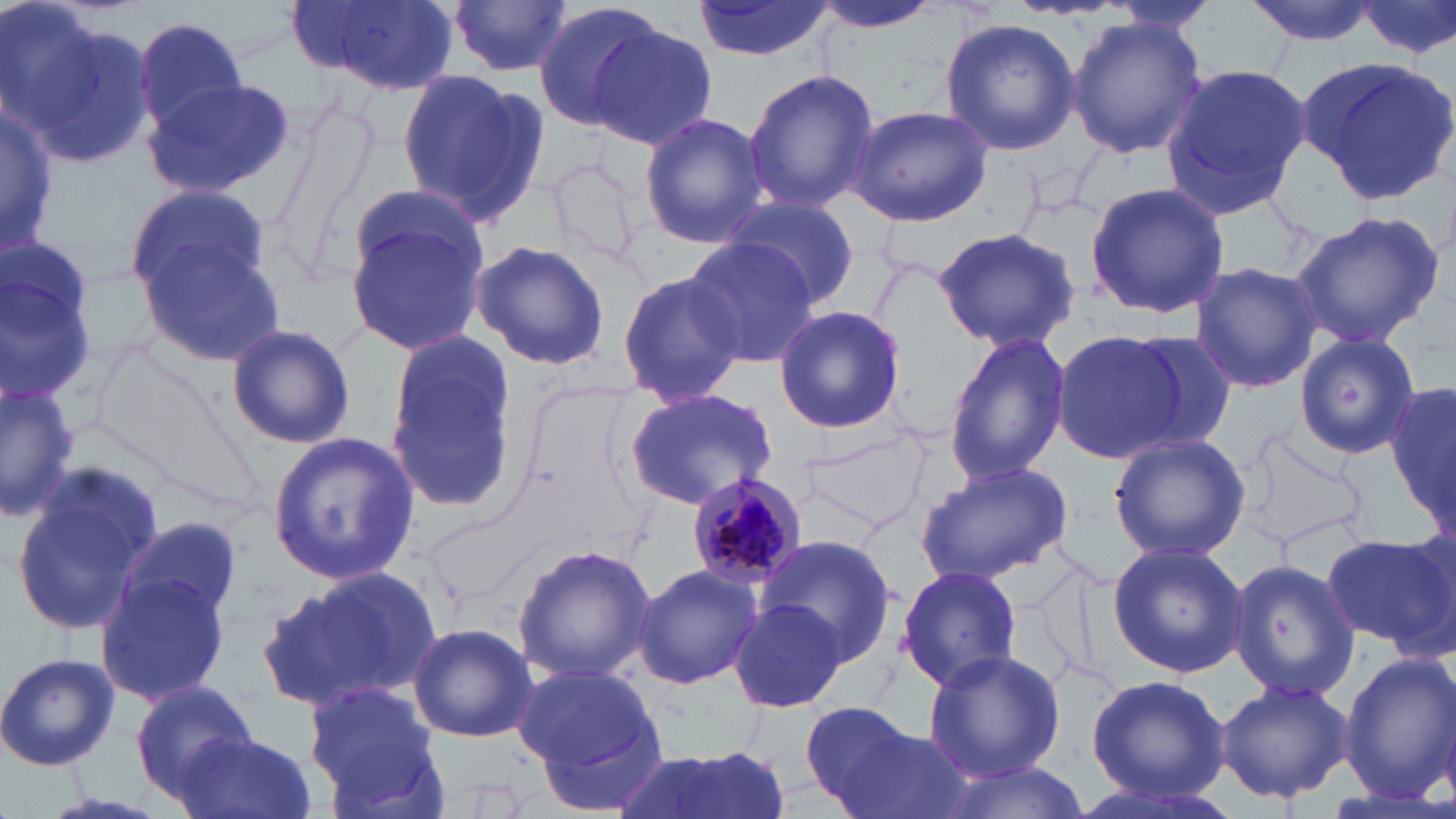
{
  "slide_level_diagnosis": "Plasmodium malariae",
  "magnification": "1000x",
  "uninfected_red_blood_cell_locations": "approximate bounding boxes as [x1, y1, x2, y2] in pixels: [298, 0, 462, 95], [693, 0, 831, 62], [810, 0, 946, 34], [1245, 0, 1384, 44], [1352, 0, 1456, 62], [451, 1, 574, 79], [1101, 1, 1219, 34], [531, 2, 668, 132], [2, 3, 158, 169], [1066, 15, 1208, 159], [133, 16, 251, 131], [940, 18, 1079, 157], [588, 23, 719, 149], [1299, 55, 1456, 205], [1160, 63, 1313, 218], [742, 68, 879, 214], [397, 69, 545, 226], [142, 78, 296, 199], [0, 97, 57, 257], [844, 105, 993, 228], [639, 112, 772, 248], [1084, 180, 1230, 319], [123, 182, 270, 304], [350, 183, 485, 284], [726, 193, 861, 310], [342, 207, 488, 358], [1288, 210, 1445, 348], [933, 227, 1084, 352], [0, 233, 103, 404], [137, 236, 291, 369], [681, 236, 818, 365], [468, 239, 610, 371], [1189, 261, 1324, 394], [617, 268, 745, 410], [772, 305, 907, 434], [225, 323, 356, 450], [1112, 330, 1238, 456], [384, 331, 516, 514], [943, 331, 1069, 486], [1049, 331, 1189, 463], [1294, 333, 1421, 461], [1388, 376, 1456, 533], [0, 381, 80, 522], [622, 387, 778, 507], [266, 431, 420, 587], [1107, 432, 1248, 564], [10, 461, 166, 637], [916, 461, 1072, 582], [116, 516, 245, 633], [1322, 531, 1456, 654], [756, 536, 897, 666], [1106, 540, 1248, 678], [512, 542, 658, 684], [1229, 558, 1358, 703], [631, 564, 763, 689], [896, 564, 1023, 691], [259, 569, 439, 715], [97, 570, 229, 707], [728, 601, 850, 713], [407, 621, 538, 744], [923, 648, 1063, 781], [1338, 651, 1455, 803], [0, 652, 120, 771], [512, 661, 668, 799], [1084, 675, 1233, 806], [1214, 677, 1354, 804], [130, 680, 263, 800], [302, 681, 447, 814], [800, 703, 953, 819], [176, 731, 317, 819], [611, 746, 783, 819], [932, 759, 1089, 819]",
  "plasmodium_malariae_infected_red_blood_cell_locations": "approximate bounding boxes as [x1, y1, x2, y2] in pixels: [684, 471, 804, 591]",
  "field_of_view": "one of a larger specimen",
  "stain": "May-Grünwald-Giemsa",
  "image_size": "1456×819 pixels",
  "preparation": "thin blood film",
  "modality": "light microscopy"
}